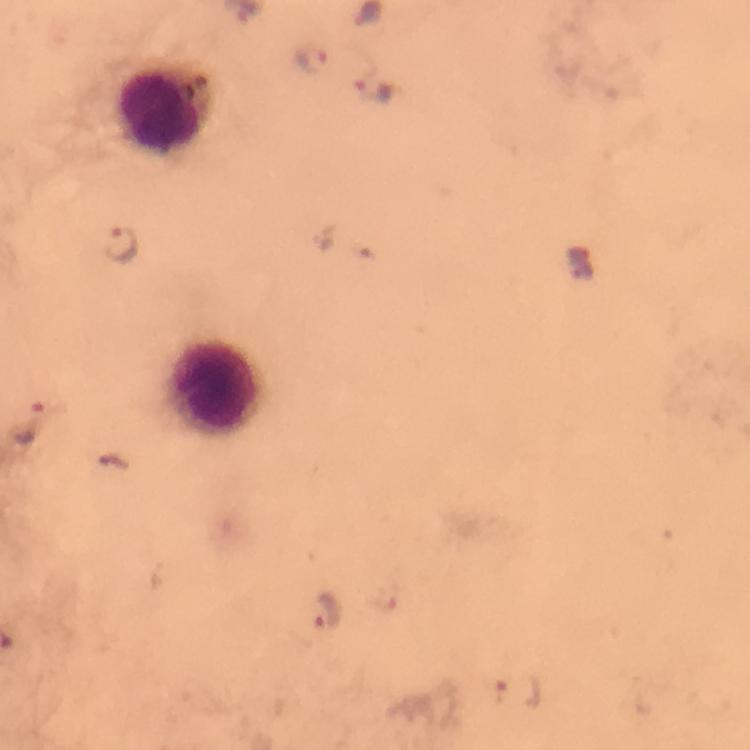

immersion oil = used
stain = Giemsa
cropped from = a single field of view
leukocyte locations = approximate centers as [x, y] in pixels: [163, 110], [215, 389]
image size = 750×750 pixels
capture = smartphone mounted on the microscope
magnification = 100x
Plasmodium parasite locations = approximate centers as [x, y] in pixels: [313, 60], [373, 90], [121, 244], [32, 425], [327, 613], [515, 689]
preparation = thick blood smear
context = from a malaria diagnostic workup